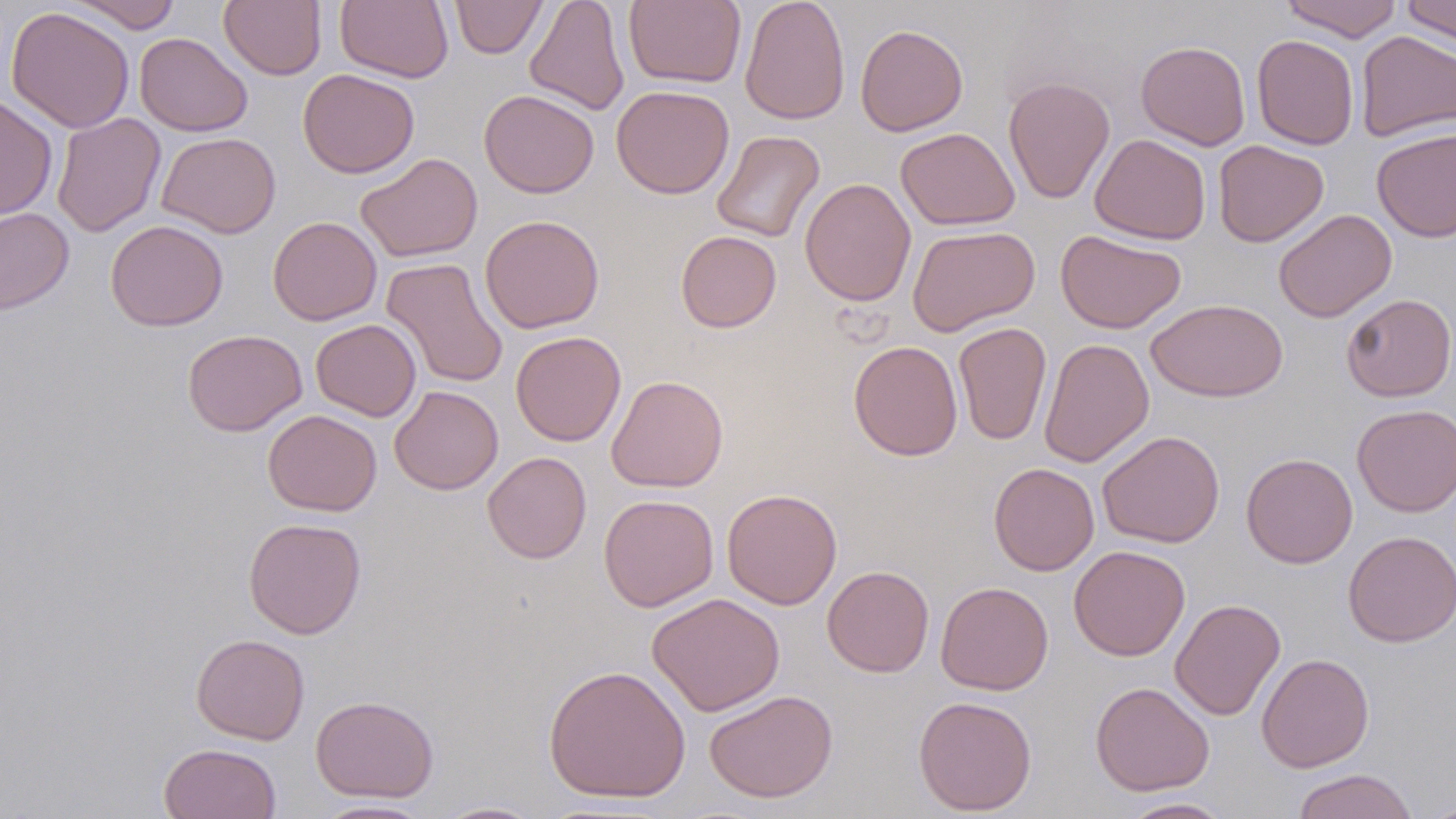
slide-level diagnosis = no evidence of blood parasites
uninfected red blood cell locations = approximate bounding boxes as [x1, y1, x2, y2] in pixels: [68, 0, 182, 34], [219, 0, 326, 80], [336, 0, 453, 83], [450, 0, 547, 59], [525, 0, 630, 116], [624, 0, 746, 88], [739, 0, 850, 126], [1280, 0, 1404, 42], [1401, 1, 1456, 46], [6, 5, 135, 134], [855, 23, 968, 136], [1355, 30, 1456, 141], [134, 32, 252, 136], [1252, 34, 1359, 150], [1135, 40, 1251, 151], [298, 68, 420, 178], [1003, 76, 1115, 204], [611, 85, 734, 199], [479, 90, 599, 198], [0, 95, 57, 221], [51, 112, 166, 238], [895, 127, 1020, 230], [1371, 128, 1456, 242], [711, 130, 825, 243], [157, 132, 281, 238], [1090, 134, 1211, 244], [1213, 140, 1329, 247], [355, 153, 482, 263], [800, 177, 916, 307], [0, 207, 74, 314], [1273, 209, 1397, 323], [479, 214, 605, 333], [267, 216, 382, 325], [105, 219, 228, 331], [907, 224, 1040, 337], [1055, 229, 1187, 334], [675, 230, 781, 332], [381, 257, 509, 389], [1340, 294, 1456, 402], [1146, 298, 1288, 402], [311, 318, 421, 421], [953, 322, 1052, 445], [182, 329, 307, 436], [511, 331, 626, 446], [1039, 338, 1155, 468], [848, 340, 963, 460], [606, 374, 729, 493], [389, 385, 504, 495], [1351, 404, 1456, 517], [262, 409, 382, 516], [1097, 430, 1225, 548], [482, 451, 592, 564], [1241, 452, 1358, 569], [988, 462, 1099, 575], [721, 488, 842, 609], [598, 494, 719, 612], [243, 517, 367, 639], [1343, 530, 1456, 647], [1068, 544, 1190, 661], [822, 565, 934, 677], [935, 581, 1053, 696], [646, 593, 785, 716], [1170, 598, 1286, 721], [190, 634, 310, 745], [1256, 652, 1375, 772], [543, 664, 691, 803], [1089, 681, 1215, 796], [703, 688, 838, 803], [310, 695, 439, 802], [912, 695, 1037, 816], [158, 743, 282, 819], [1292, 768, 1419, 819], [1116, 797, 1236, 818], [1420, 797, 1456, 819], [311, 799, 437, 818], [434, 801, 546, 818]
magnification = 1000x
modality = light microscopy
preparation = thin blood smear
field of view = single
stain = May-Grünwald-Giemsa
image size = 1456×819 pixels